Describe the morphology of the red blood cells.
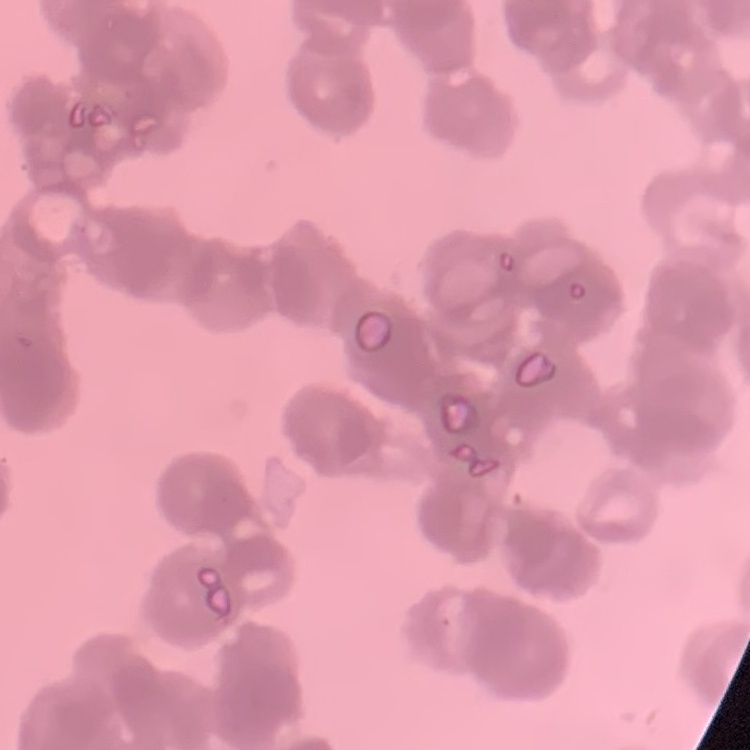
They show rouleaux formation.

Summary:
  - Image type: one tile cut from a larger photomicrograph
  - Stain: Field's or Giemsa
  - Preparation: thin blood smear